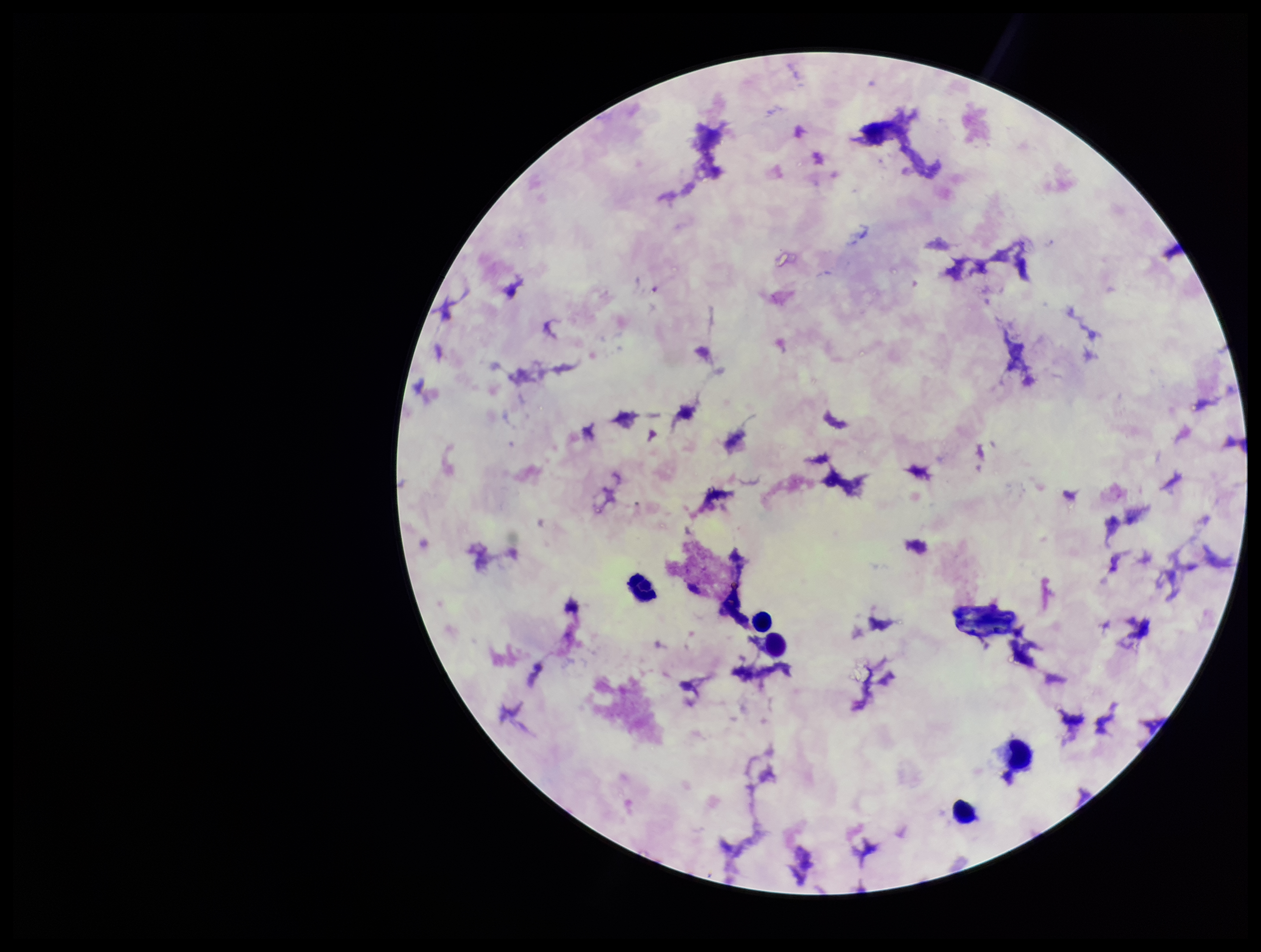

Summary:
  - Capture: smartphone photograph through the microscope eyepiece
  - Parasite count: 0
  - Preparation: thick
  - Stain: Giemsa
  - Plasmodium parasites: none detected
  - Patient malaria status: negative
  - Image size: 1261×952 pixels
  - Leukocyte count: 4
  - Field of view: single